Classify this cell by malaria status.
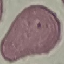

Uninfected.

{
  "image_type": "automatically extracted cell patch, resized to 64 × 64 pixels",
  "capture": "smartphone through the microscope eyepiece",
  "preparation": "thin blood smear",
  "stain": "Giemsa"
}